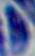 Toxoplasma gondii is seen. Photomicrograph. 1000x magnification.